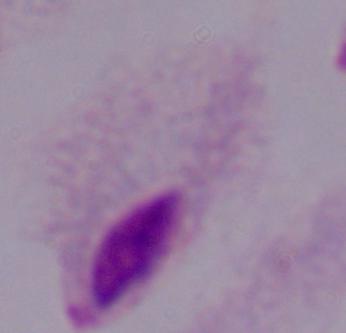 Captured at 1000x magnification. Photomicrograph. A trichomonad is seen.